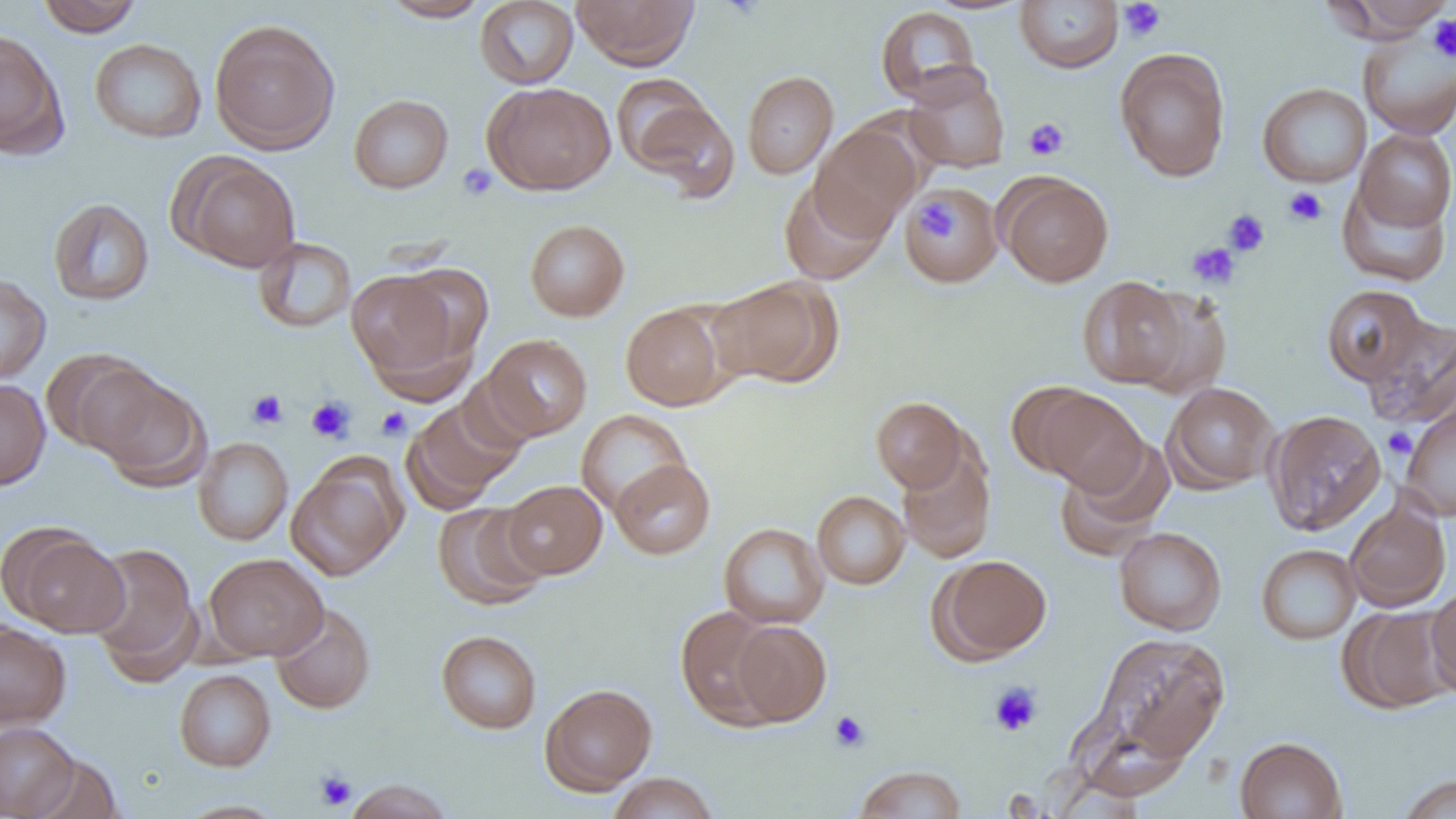
Summary:
  - Coordinate format: approximate bounding boxes as (x1,y1)-(x2,y2) corner pairs in pixels
  - Uninfected red blood cell locations: (36,0)-(143,36), (380,0)-(491,21), (475,0)-(578,89), (572,0)-(699,70), (1015,0)-(1123,73), (1328,1)-(1456,39), (875,6)-(982,105), (209,19)-(340,154), (0,27)-(68,157), (1358,30)-(1456,140), (90,38)-(206,143), (1115,48)-(1231,183), (904,64)-(1010,174), (742,70)-(838,179), (611,73)-(713,173), (483,82)-(616,195), (1258,83)-(1371,188), (349,94)-(453,193), (634,99)-(739,203), (810,124)-(921,238), (1354,128)-(1455,232), (178,155)-(300,272), (999,174)-(1114,287), (779,178)-(889,285), (1336,179)-(1452,287), (902,184)-(1002,288), (48,198)-(154,306), (525,219)-(630,321), (253,237)-(356,333), (393,263)-(494,364), (345,270)-(464,387), (0,273)-(51,385), (1078,276)-(1190,389), (707,277)-(841,388), (1322,284)-(1430,387), (1132,287)-(1232,400), (621,303)-(731,411), (1363,316)-(1456,430), (482,334)-(592,440), (41,348)-(159,456), (88,370)-(210,491), (0,379)-(51,490), (1163,382)-(1278,492), (1023,386)-(1148,496), (871,397)-(968,493), (402,398)-(524,512), (1400,403)-(1456,521), (576,409)-(691,515), (1264,409)-(1386,535), (194,437)-(293,545), (1055,437)-(1175,559), (897,445)-(996,563), (610,458)-(716,559), (286,459)-(405,580), (502,480)-(607,579), (812,491)-(910,589), (1344,498)-(1451,612), (433,501)-(550,610), (718,523)-(829,629), (1113,527)-(1227,635), (8,528)-(129,637), (85,542)-(201,682), (1256,544)-(1361,645), (204,553)-(328,661), (934,554)-(1052,662), (1426,584)-(1456,697), (271,603)-(375,714), (1339,605)-(1454,714), (675,606)-(780,727), (0,620)-(71,728), (730,620)-(832,726), (436,630)-(542,734), (1092,631)-(1231,765), (174,669)-(275,771), (540,683)-(656,795), (0,722)-(80,818), (1235,736)-(1347,819), (28,754)-(124,819), (854,765)-(966,818), (608,772)-(718,819), (1396,775)-(1456,819), (343,779)-(455,819), (175,800)-(287,818)
  - Platelet locations: (1119,1)-(1166,42), (1429,14)-(1456,63), (1023,117)-(1070,160), (457,162)-(497,201), (1283,187)-(1328,226), (913,197)-(960,244), (1223,209)-(1270,257), (1187,242)-(1239,288), (247,389)-(289,430), (306,396)-(356,443), (376,407)-(412,440), (1383,427)-(1417,458), (989,682)-(1042,736), (829,710)-(870,752), (314,770)-(358,811)
  - Slide-level diagnosis: no evidence of blood parasites
  - Image size: 1456×819 pixels
  - Field of view: single
  - Preparation: thin blood film
  - Modality: optical microscopy
  - Magnification: 1000x